Locate and identify every blood parasite.
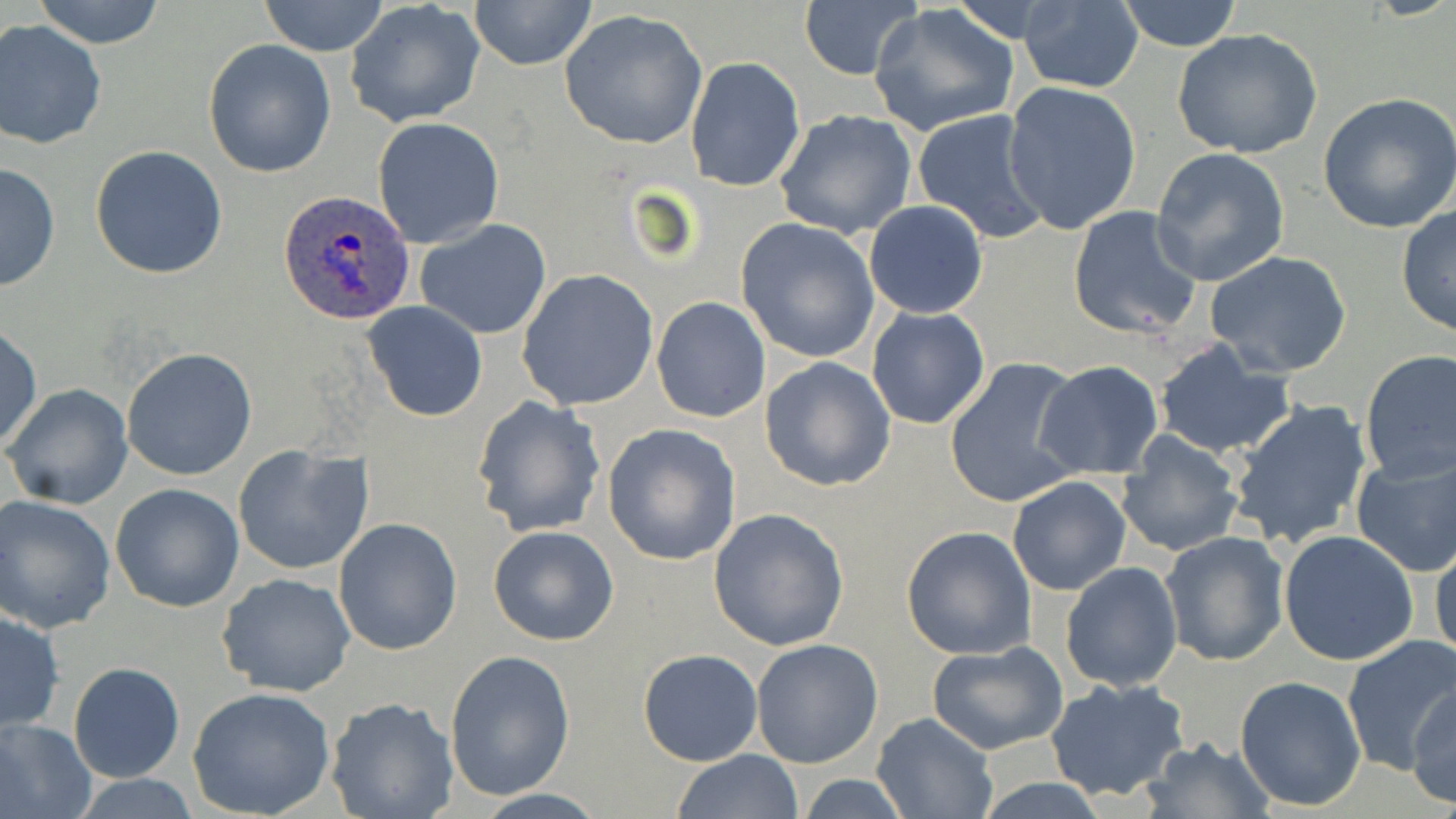

Approximate bounding boxes as named x1/y1/x2/y2 corners in pixels.
Plasmodium ovale-infected red blood cells: (x1=277, y1=188, x2=416, y2=326).
No Plasmodium falciparum, Plasmodium malariae, Plasmodium vivax, Babesia divergens, or Trypanosoma brucei observed.

Summary:
  - Uninfected red blood cell locations: (x1=28, y1=0, x2=168, y2=48), (x1=469, y1=0, x2=597, y2=72), (x1=1114, y1=0, x2=1245, y2=51), (x1=256, y1=1, x2=390, y2=56), (x1=1018, y1=1, x2=1144, y2=94), (x1=347, y1=2, x2=485, y2=128), (x1=799, y1=2, x2=923, y2=80), (x1=868, y1=3, x2=1021, y2=140), (x1=558, y1=9, x2=708, y2=151), (x1=0, y1=20, x2=106, y2=149), (x1=1172, y1=27, x2=1322, y2=160), (x1=202, y1=38, x2=337, y2=177), (x1=686, y1=55, x2=806, y2=192), (x1=1003, y1=80, x2=1141, y2=236), (x1=1318, y1=92, x2=1456, y2=233), (x1=913, y1=108, x2=1052, y2=245), (x1=774, y1=110, x2=919, y2=242), (x1=372, y1=117, x2=506, y2=250), (x1=90, y1=146, x2=228, y2=280), (x1=1150, y1=147, x2=1292, y2=286), (x1=0, y1=160, x2=61, y2=294), (x1=863, y1=200, x2=989, y2=319), (x1=1066, y1=205, x2=1202, y2=340), (x1=1395, y1=206, x2=1456, y2=336), (x1=737, y1=217, x2=881, y2=363), (x1=413, y1=220, x2=553, y2=338), (x1=1205, y1=250, x2=1353, y2=379), (x1=517, y1=269, x2=660, y2=411), (x1=651, y1=296, x2=772, y2=424), (x1=361, y1=301, x2=488, y2=422), (x1=866, y1=306, x2=991, y2=429), (x1=1, y1=324, x2=42, y2=451), (x1=1152, y1=339, x2=1298, y2=458), (x1=122, y1=347, x2=258, y2=481), (x1=1358, y1=351, x2=1456, y2=483), (x1=759, y1=356, x2=896, y2=490), (x1=943, y1=356, x2=1086, y2=508), (x1=1034, y1=360, x2=1164, y2=481), (x1=3, y1=382, x2=133, y2=510), (x1=470, y1=395, x2=607, y2=539), (x1=1224, y1=399, x2=1373, y2=549), (x1=603, y1=424, x2=741, y2=566), (x1=1116, y1=432, x2=1244, y2=558), (x1=232, y1=444, x2=373, y2=576), (x1=1350, y1=449, x2=1456, y2=578), (x1=1007, y1=476, x2=1131, y2=594), (x1=110, y1=483, x2=246, y2=613), (x1=2, y1=495, x2=117, y2=632), (x1=709, y1=508, x2=848, y2=651), (x1=332, y1=518, x2=462, y2=656), (x1=901, y1=525, x2=1037, y2=660), (x1=488, y1=526, x2=619, y2=645), (x1=1278, y1=529, x2=1421, y2=667), (x1=1161, y1=531, x2=1292, y2=667), (x1=1429, y1=536, x2=1456, y2=670), (x1=1060, y1=560, x2=1184, y2=692), (x1=217, y1=572, x2=356, y2=698), (x1=0, y1=609, x2=65, y2=733), (x1=1340, y1=635, x2=1454, y2=774), (x1=751, y1=637, x2=883, y2=768), (x1=927, y1=641, x2=1069, y2=755), (x1=444, y1=648, x2=576, y2=801), (x1=638, y1=648, x2=763, y2=765), (x1=69, y1=661, x2=186, y2=784), (x1=1044, y1=676, x2=1191, y2=802), (x1=1235, y1=676, x2=1369, y2=812), (x1=1408, y1=683, x2=1455, y2=808), (x1=187, y1=687, x2=338, y2=818), (x1=325, y1=696, x2=459, y2=819), (x1=871, y1=712, x2=997, y2=817), (x1=0, y1=717, x2=96, y2=819), (x1=1141, y1=737, x2=1273, y2=817), (x1=672, y1=750, x2=804, y2=819), (x1=795, y1=774, x2=914, y2=816), (x1=976, y1=779, x2=1113, y2=817)
  - Slide-level diagnosis: Plasmodium ovale
  - Image size: 1456×819 pixels
  - Magnification: 1000x
  - Preparation: thin blood smear
  - Field of view: single
  - Modality: light microscopy
  - Stain: May-Grünwald-Giemsa